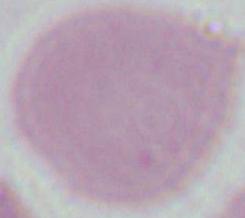
identification = red blood cell
magnification = 1000x
modality = micrograph